Identify the blood parasite species.
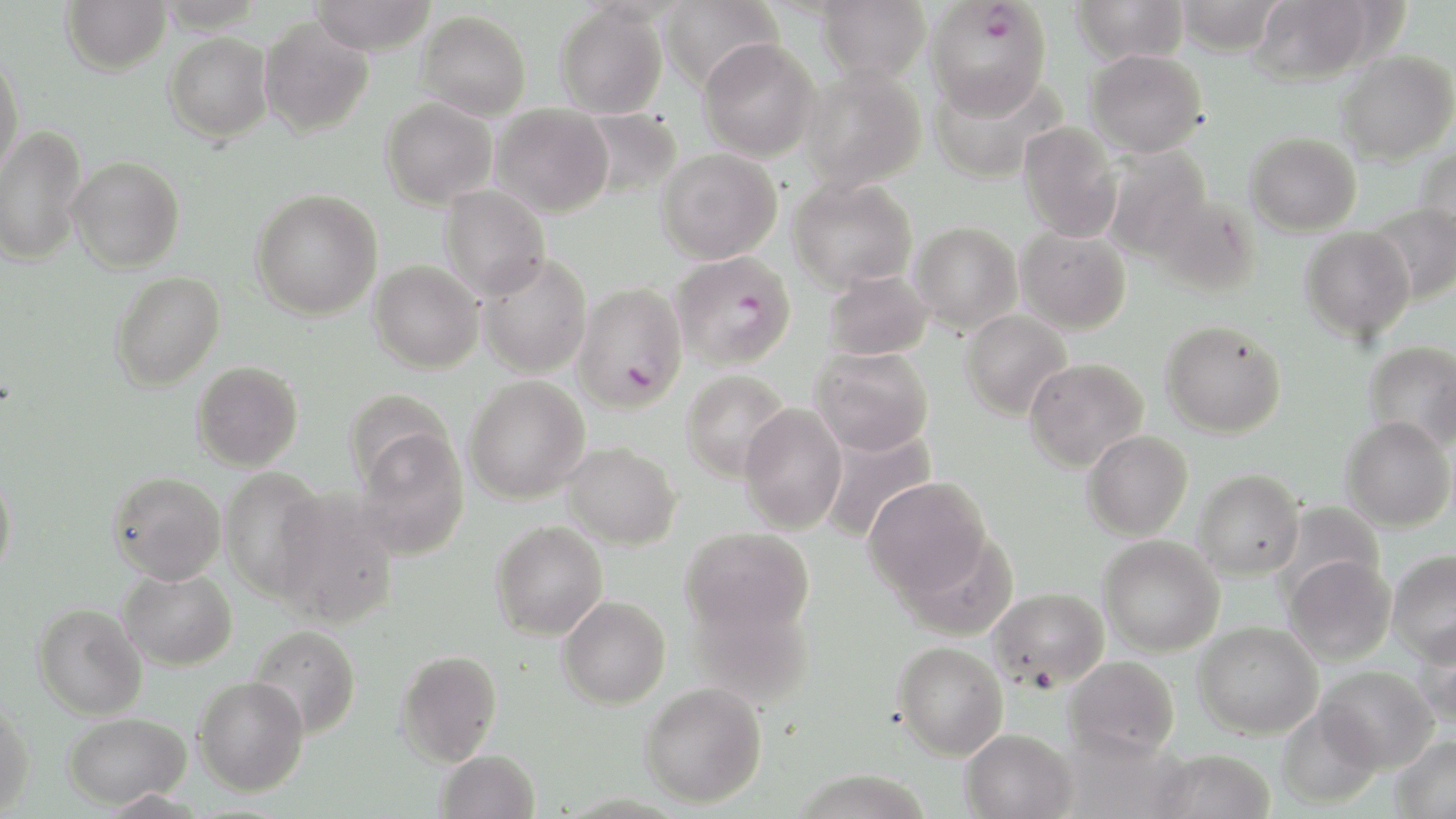
Plasmodium falciparum.

Approximate bounding boxes as (x1,y1)-(x2,y2) corner pairs in pixels. Plasmodium falciparum-infected red blood cell locations: (925,1)-(1053,120), (672,251)-(796,370), (572,282)-(688,413). Uninfected red blood cell locations: (62,0)-(171,75), (308,0)-(437,55), (660,0)-(783,93), (815,0)-(931,83), (1070,0)-(1191,65), (1173,0)-(1287,55), (1251,0)-(1373,85), (555,4)-(667,118), (417,10)-(531,121), (259,17)-(373,138), (165,32)-(273,142), (698,38)-(820,162), (1086,47)-(1208,158), (1337,50)-(1456,164), (0,54)-(24,179), (800,65)-(926,191), (929,67)-(1065,184), (381,97)-(497,209), (490,104)-(614,217), (579,108)-(682,201), (1017,121)-(1123,243), (0,125)-(87,266), (1245,131)-(1362,236), (1415,145)-(1456,253), (1101,146)-(1214,261), (656,148)-(783,264), (68,156)-(185,273), (789,176)-(918,293), (440,185)-(550,301), (251,189)-(383,320), (1149,194)-(1260,298), (1367,204)-(1456,304), (910,221)-(1022,333), (1016,226)-(1131,334), (1300,226)-(1415,342), (477,252)-(592,379), (369,260)-(483,373), (823,269)-(933,360), (110,271)-(225,391), (959,310)-(1073,421), (1161,320)-(1286,438), (1364,340)-(1456,452), (810,346)-(934,456), (1024,357)-(1148,472), (192,360)-(303,471), (681,369)-(791,482), (464,376)-(590,504), (343,387)-(455,494), (738,404)-(848,534), (1341,417)-(1454,533), (818,428)-(939,545), (1082,430)-(1193,541), (356,431)-(470,561), (561,441)-(681,550), (218,468)-(329,600), (1193,469)-(1305,580), (108,471)-(226,585), (0,473)-(16,580), (864,477)-(993,603), (271,489)-(399,628), (1276,501)-(1386,603), (491,521)-(608,641), (680,527)-(814,641), (1098,535)-(1225,657), (1387,549)-(1456,664), (1284,555)-(1396,665), (118,568)-(237,671), (989,586)-(1109,690), (687,590)-(816,709), (558,595)-(671,709), (32,603)-(147,720), (1194,621)-(1322,739), (1416,623)-(1456,726), (248,624)-(361,739), (892,641)-(1008,760), (396,649)-(502,767), (1065,655)-(1180,762), (1316,665)-(1437,772), (193,675)-(310,796), (640,681)-(767,808), (0,700)-(35,818), (1276,705)-(1384,810), (63,712)-(191,808), (961,729)-(1078,819), (1389,734)-(1456,818), (1151,748)-(1277,819), (435,750)-(540,819), (793,768)-(934,819). Light microscopy. Thin blood film. May-Grünwald-Giemsa-stained preparation. 1000x magnification. Image is 1456×819 pixels. Single field of view.